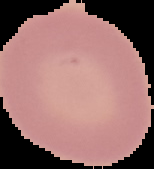

Cell region segmented out of the field of view; the surrounding area is masked to black. Malaria status: uninfected. From a thin blood film. Image is 154×169 pixels.